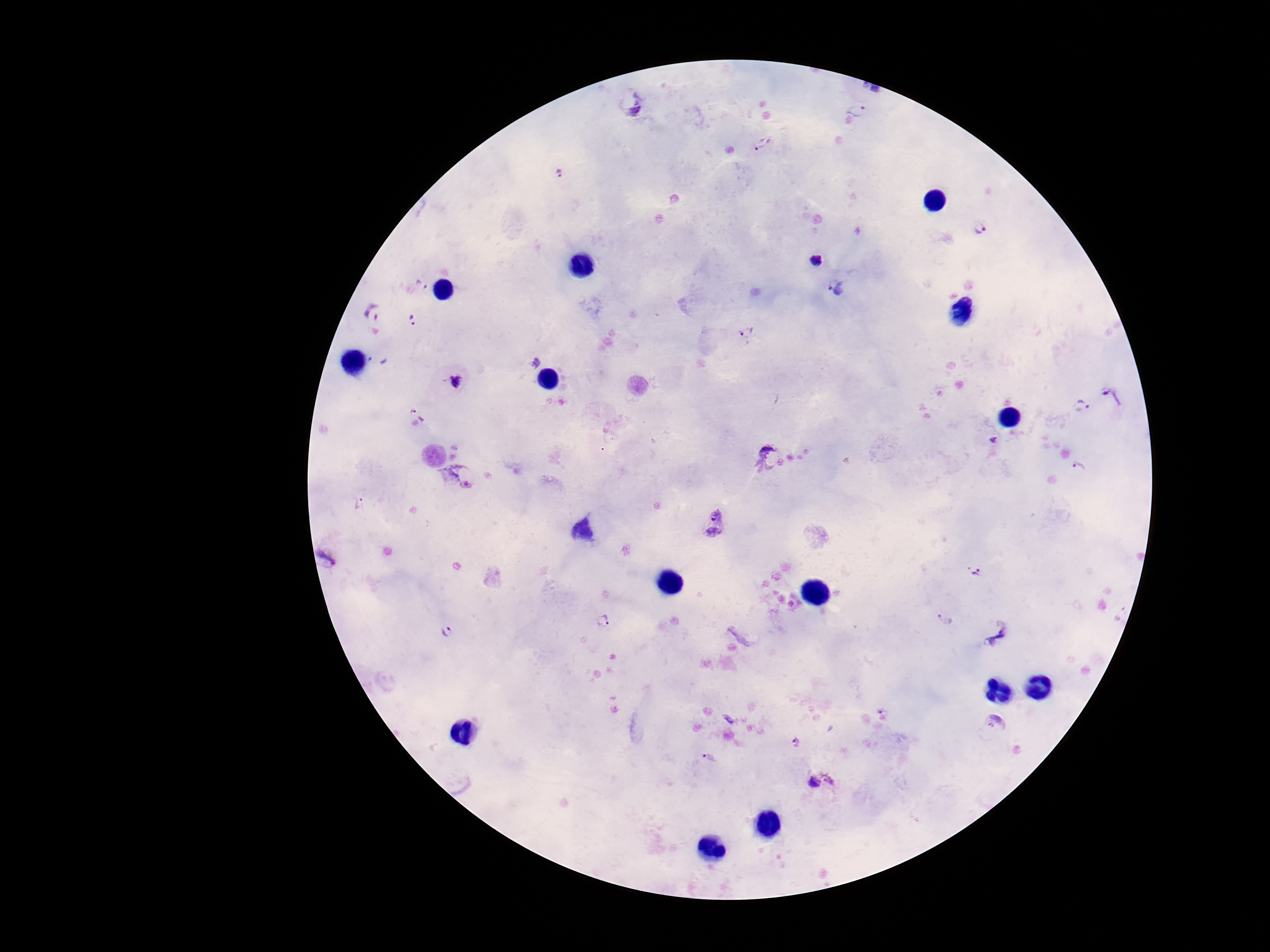
Approximate centers as {x, y} in pixels. Plasmodium parasite locations: {632, 104}, {856, 107}, {764, 145}, {562, 174}, {981, 229}, {815, 260}, {422, 286}, {838, 287}, {373, 314}, {412, 319}, {746, 334}, {378, 359}, {533, 364}, {456, 382}, {1116, 396}, {1082, 409}, {411, 411}, {994, 440}, {770, 457}, {1079, 470}, {456, 477}, {359, 504}, {714, 525}, {327, 557}, {976, 572}, {605, 620}, {945, 620}, {447, 632}, {999, 637}, {996, 725}, {798, 743}, {709, 758}, {823, 782}. Smartphone photograph taken through the microscope eyepiece. Image is 1270×952 pixels. Giemsa-stained preparation. 100x magnification. Patient malaria status: positive. Single field of view. Thick blood film.